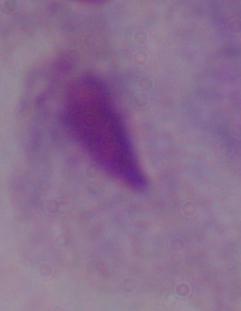
Summary:
  - Modality: micrograph
  - Identification: trichomonad
  - Magnification: 1000x